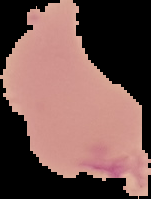
Summary:
  - Result: no Plasmodium parasites detected
  - Image type: segmented cell region with the area outside set to black
  - Preparation: thin blood smear
  - Image size: 151×199 pixels